Give the preparation type.
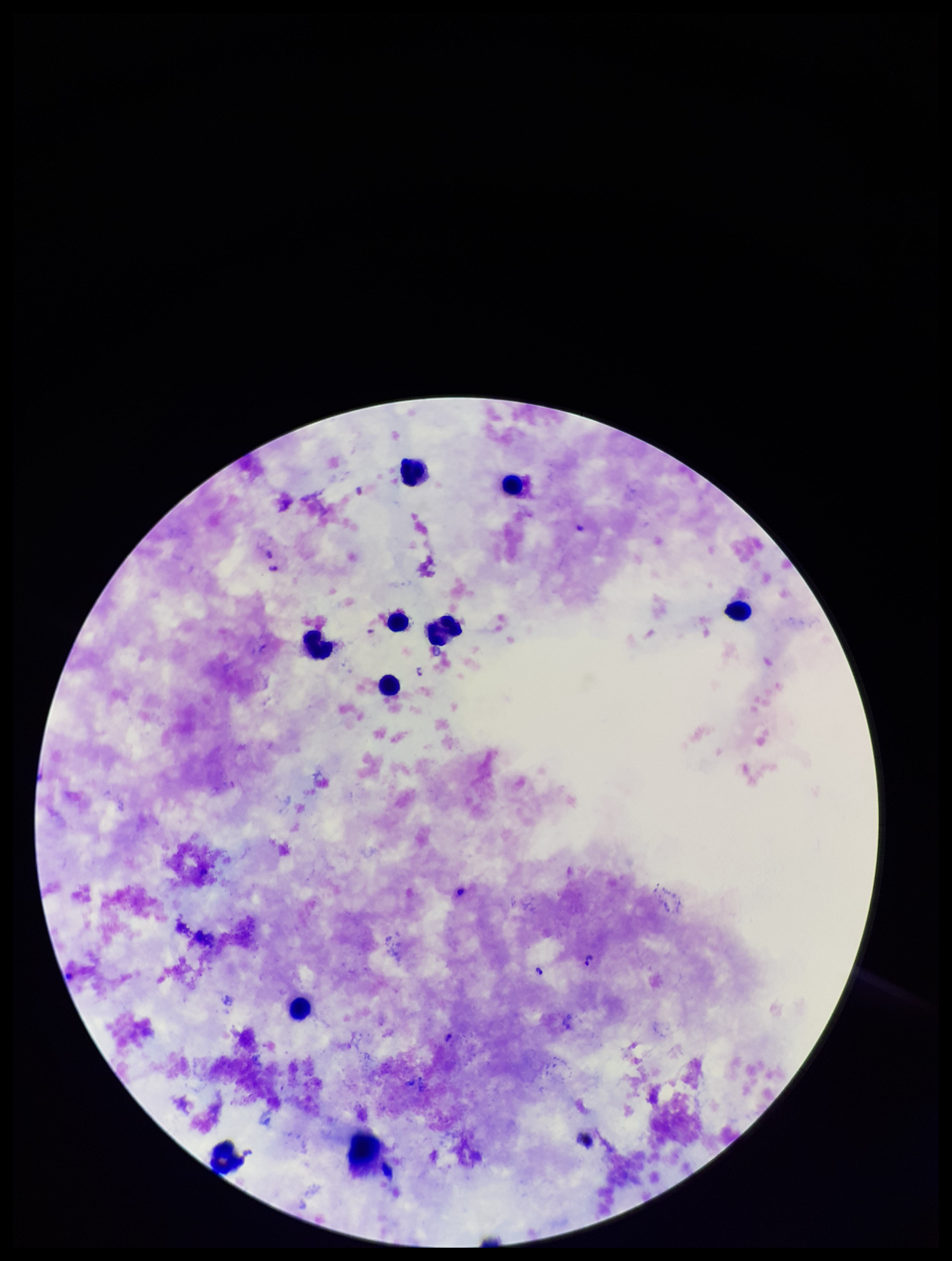
A thick smear.

Summary:
  - Plasmodium parasites: seen
  - Stain: Giemsa
  - Capture: smartphone photograph through the microscope eyepiece
  - Image size: 952×1261 pixels
  - Parasite count: 5
  - Field of view: one from this slide
  - Species reported for this patient: Plasmodium falciparum
  - Patient malaria status: infected
  - Leukocyte count: 10